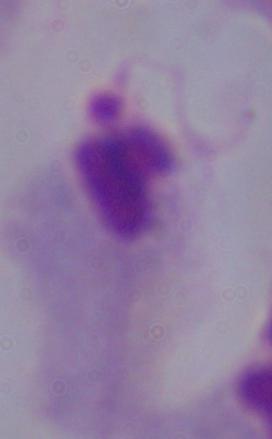

Summary:
  - Modality: micrograph
  - Identification: trichomonad
  - Magnification: 1000x